Classify this cell by malaria status.
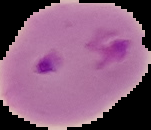
It is parasitized.

Summary:
  - Image size: 151×130 pixels
  - Preparation: thin blood film
  - Image type: segmented cell region on a black background